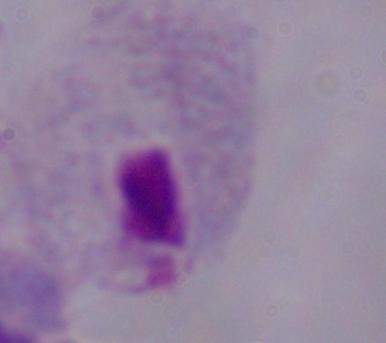

modality: micrograph
magnification: 1000x
identification: trichomonad